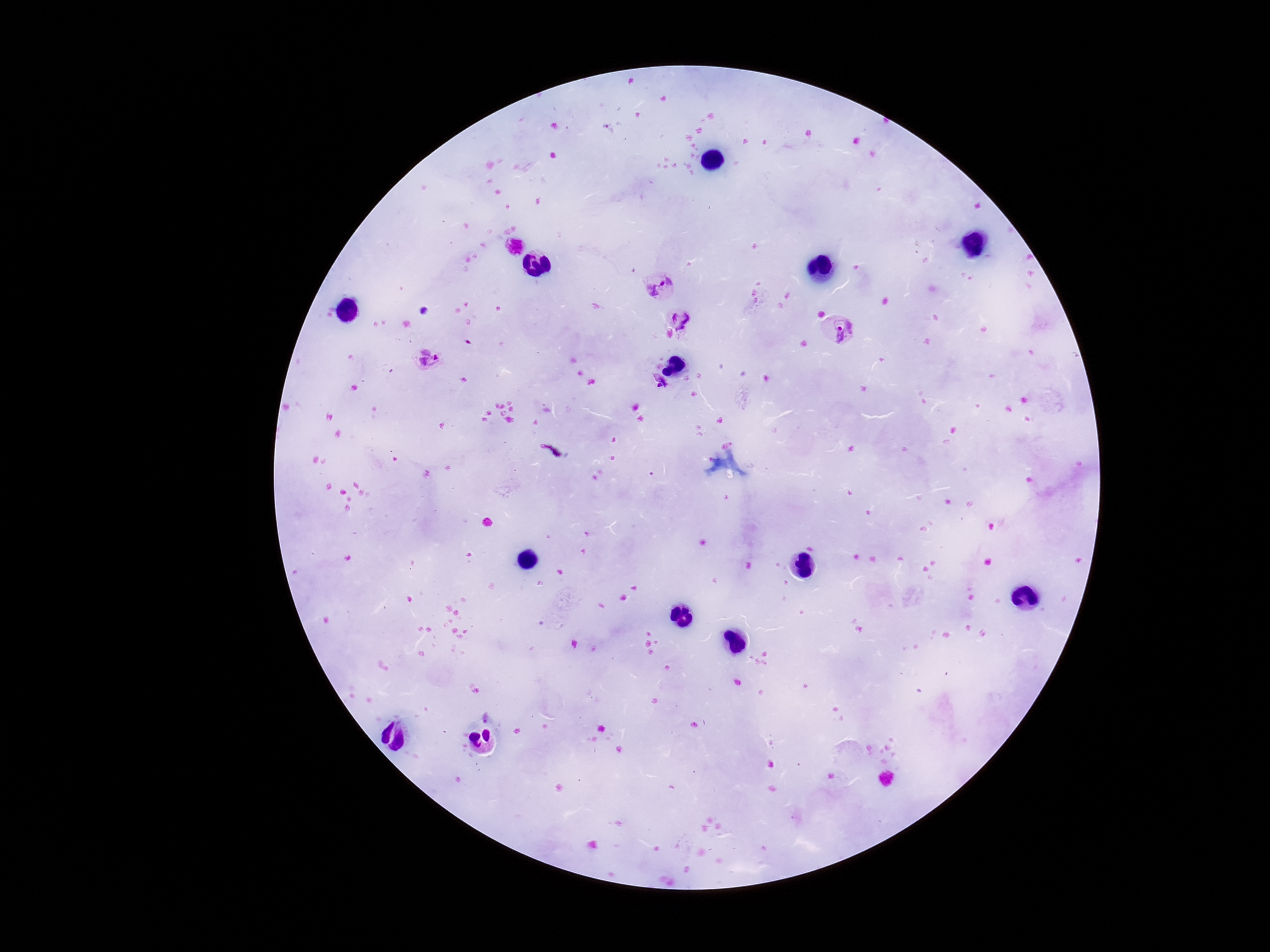

Approximate centers as {x, y} in pixels. Plasmodium parasite locations: {661, 286}, {681, 320}, {841, 329}, {429, 362}, {657, 383}, {550, 450}. Thick peripheral-blood smear. Smartphone photograph taken through the microscope eyepiece. Image is 1270×952 pixels. Patient malaria status: positive. Giemsa-stained preparation. 100x magnification. Single field of view.